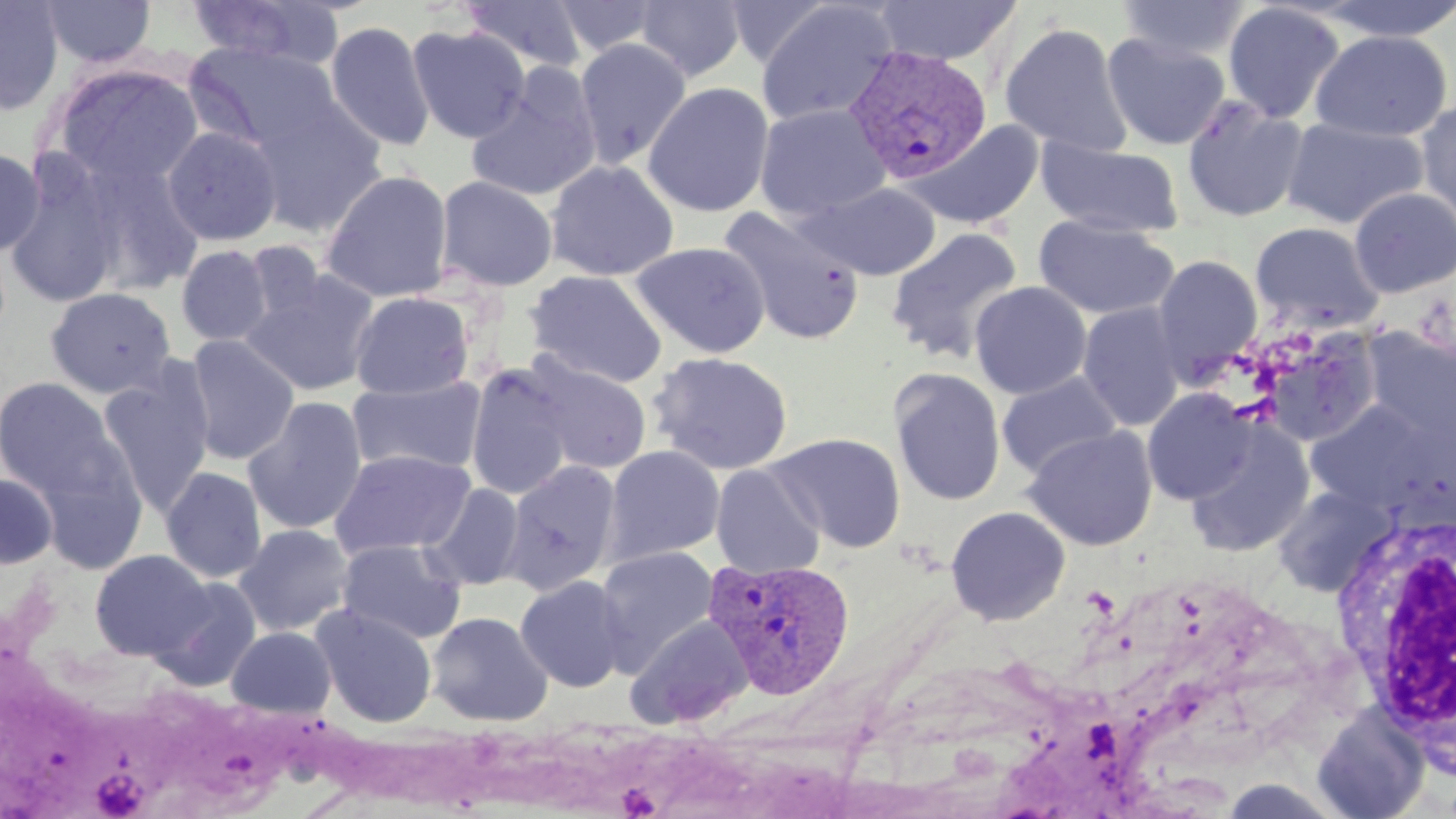

Summary:
  - Coordinate format: approximate bounding boxes as (x1, y1, x2, y2) in pixels
  - Uninfected red blood cell locations: (40, 0, 156, 69), (184, 0, 346, 69), (552, 0, 662, 57), (723, 0, 837, 69), (755, 0, 900, 126), (875, 0, 1022, 66), (1115, 0, 1250, 61), (1315, 0, 1456, 42), (0, 1, 65, 116), (460, 1, 588, 75), (634, 1, 748, 82), (1222, 2, 1346, 124), (325, 20, 435, 152), (999, 22, 1132, 157), (406, 24, 531, 142), (1311, 29, 1451, 141), (1101, 32, 1231, 151), (573, 38, 691, 168), (186, 41, 341, 155), (49, 62, 205, 192), (465, 66, 603, 204), (642, 82, 775, 217), (245, 95, 387, 237), (1182, 95, 1310, 223), (1415, 96, 1456, 231), (754, 104, 890, 221), (1281, 117, 1429, 229), (908, 120, 1044, 230), (162, 126, 283, 246), (1036, 138, 1184, 238), (0, 148, 45, 257), (4, 155, 128, 310), (75, 156, 206, 297), (546, 160, 679, 281), (320, 169, 454, 303), (434, 175, 558, 292), (801, 181, 941, 280), (1349, 187, 1456, 298), (718, 205, 865, 346), (1034, 215, 1178, 321), (1250, 222, 1384, 332), (885, 226, 1023, 363), (244, 240, 327, 327), (630, 241, 771, 358), (176, 245, 274, 346), (1152, 255, 1264, 382), (244, 269, 380, 396), (526, 270, 667, 389), (969, 281, 1092, 399), (45, 287, 176, 399), (350, 291, 474, 400), (1077, 301, 1186, 433), (1362, 328, 1456, 448), (1255, 329, 1385, 447), (183, 335, 300, 465), (649, 351, 794, 475), (522, 355, 652, 474), (97, 362, 215, 515), (466, 367, 576, 501), (890, 368, 1006, 506), (996, 371, 1122, 480), (346, 376, 487, 477), (0, 377, 121, 501), (1142, 389, 1255, 504), (243, 396, 367, 536), (1304, 400, 1447, 512), (1184, 420, 1315, 557), (1022, 425, 1158, 551), (30, 432, 148, 571), (769, 432, 906, 554), (604, 445, 725, 565), (329, 449, 476, 559), (501, 460, 621, 595), (711, 463, 824, 580), (160, 467, 267, 583), (0, 471, 59, 570), (423, 482, 525, 590), (1272, 485, 1397, 597), (945, 505, 1071, 626), (233, 524, 355, 637), (337, 539, 468, 644), (594, 546, 718, 673), (90, 549, 213, 660), (148, 575, 263, 691), (515, 575, 631, 692), (311, 604, 438, 728), (427, 611, 553, 726), (626, 615, 754, 728), (225, 625, 337, 719), (1311, 704, 1430, 819)
  - Plasmodium vivax-infected red blood cell locations: (843, 46, 993, 185), (704, 557, 855, 700)
  - Platelet locations: (91, 767, 150, 816)
  - White blood cell locations: (1326, 506, 1456, 762)
  - Slide-level diagnosis: Plasmodium vivax
  - Image size: 1456×819 pixels
  - Modality: optical microscopy
  - Field of view: one of a larger specimen
  - Preparation: thin blood film
  - Stain: May-Grünwald-Giemsa
  - Magnification: 1000x